State the blood parasite species.
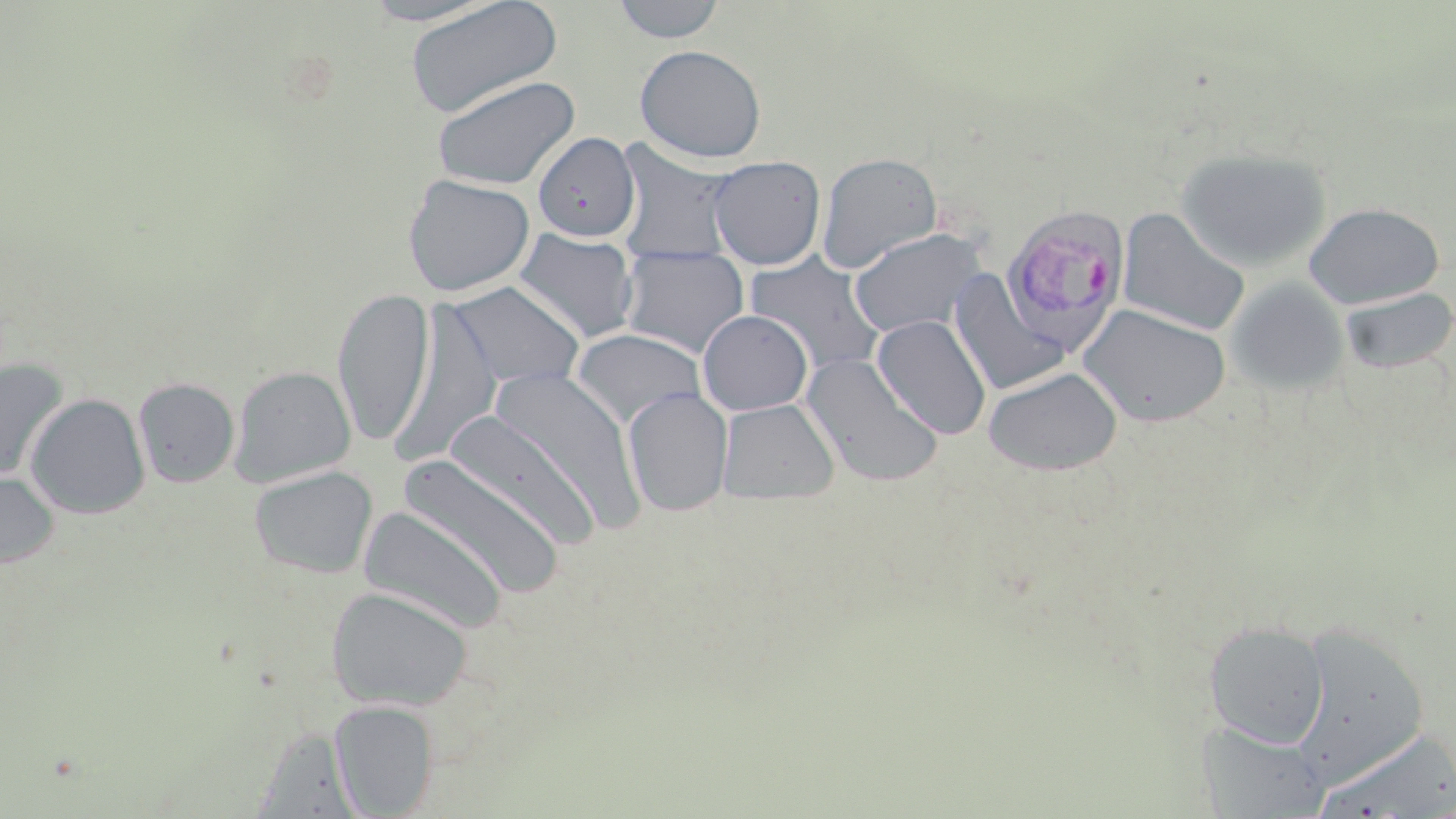

Plasmodium vivax.

field of view = single
modality = light microscopy
Plasmodium vivax-infected red blood cell locations = approximate bounding boxes as named x1/y1/x2/y2 corners in pixels: (x1=1002, y1=205, x2=1131, y2=354)
uninfected red blood cell locations = approximate bounding boxes as named x1/y1/x2/y2 corners in pixels: (x1=357, y1=0, x2=505, y2=26), (x1=403, y1=0, x2=563, y2=119), (x1=610, y1=0, x2=728, y2=44), (x1=635, y1=44, x2=767, y2=163), (x1=430, y1=74, x2=580, y2=190), (x1=532, y1=132, x2=640, y2=242), (x1=612, y1=141, x2=742, y2=262), (x1=1174, y1=148, x2=1332, y2=273), (x1=816, y1=152, x2=943, y2=273), (x1=707, y1=156, x2=826, y2=270), (x1=402, y1=174, x2=535, y2=297), (x1=1304, y1=202, x2=1445, y2=309), (x1=1117, y1=208, x2=1251, y2=337), (x1=848, y1=227, x2=986, y2=338), (x1=513, y1=228, x2=640, y2=345), (x1=618, y1=247, x2=751, y2=359), (x1=744, y1=253, x2=886, y2=375), (x1=948, y1=270, x2=1070, y2=396), (x1=1225, y1=277, x2=1350, y2=396), (x1=446, y1=281, x2=585, y2=391), (x1=332, y1=286, x2=434, y2=447), (x1=1340, y1=287, x2=1456, y2=374), (x1=388, y1=302, x2=504, y2=466), (x1=1077, y1=303, x2=1231, y2=427), (x1=697, y1=310, x2=813, y2=416), (x1=872, y1=315, x2=992, y2=440), (x1=570, y1=328, x2=706, y2=429), (x1=800, y1=353, x2=944, y2=488), (x1=0, y1=357, x2=69, y2=481), (x1=230, y1=365, x2=355, y2=488), (x1=483, y1=365, x2=646, y2=538), (x1=983, y1=367, x2=1121, y2=475), (x1=133, y1=377, x2=239, y2=488), (x1=623, y1=387, x2=733, y2=517), (x1=26, y1=393, x2=150, y2=519), (x1=716, y1=398, x2=839, y2=504), (x1=443, y1=409, x2=601, y2=551), (x1=398, y1=454, x2=566, y2=600), (x1=249, y1=465, x2=378, y2=579), (x1=0, y1=471, x2=59, y2=570), (x1=358, y1=505, x2=510, y2=635), (x1=326, y1=586, x2=472, y2=711), (x1=1203, y1=621, x2=1331, y2=748), (x1=1295, y1=623, x2=1429, y2=779), (x1=330, y1=700, x2=438, y2=817), (x1=1197, y1=720, x2=1330, y2=817), (x1=1315, y1=727, x2=1455, y2=817)
stain = May-Grünwald-Giemsa
preparation = thin blood film
magnification = 1000x
image size = 1456×819 pixels